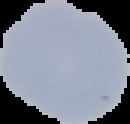 Cell region segmented out of the field of view; the surrounding area is masked to black. Malaria status: uninfected. From a thin blood smear. Image is 130×124 pixels.